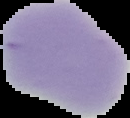
Summary:
  - Malaria status: uninfected
  - Image type: segmented cell region on a black background
  - Preparation: thin blood smear
  - Image size: 130×118 pixels